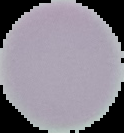
image type = segmented cell region on a black background
result = no malaria parasites seen
image size = 124×133 pixels
preparation = thin blood film